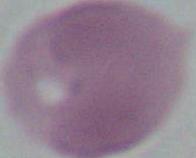

Summary:
  - Identification: red blood cell
  - Magnification: 1000x
  - Modality: photomicrograph